Point out each Plasmodium parasite.
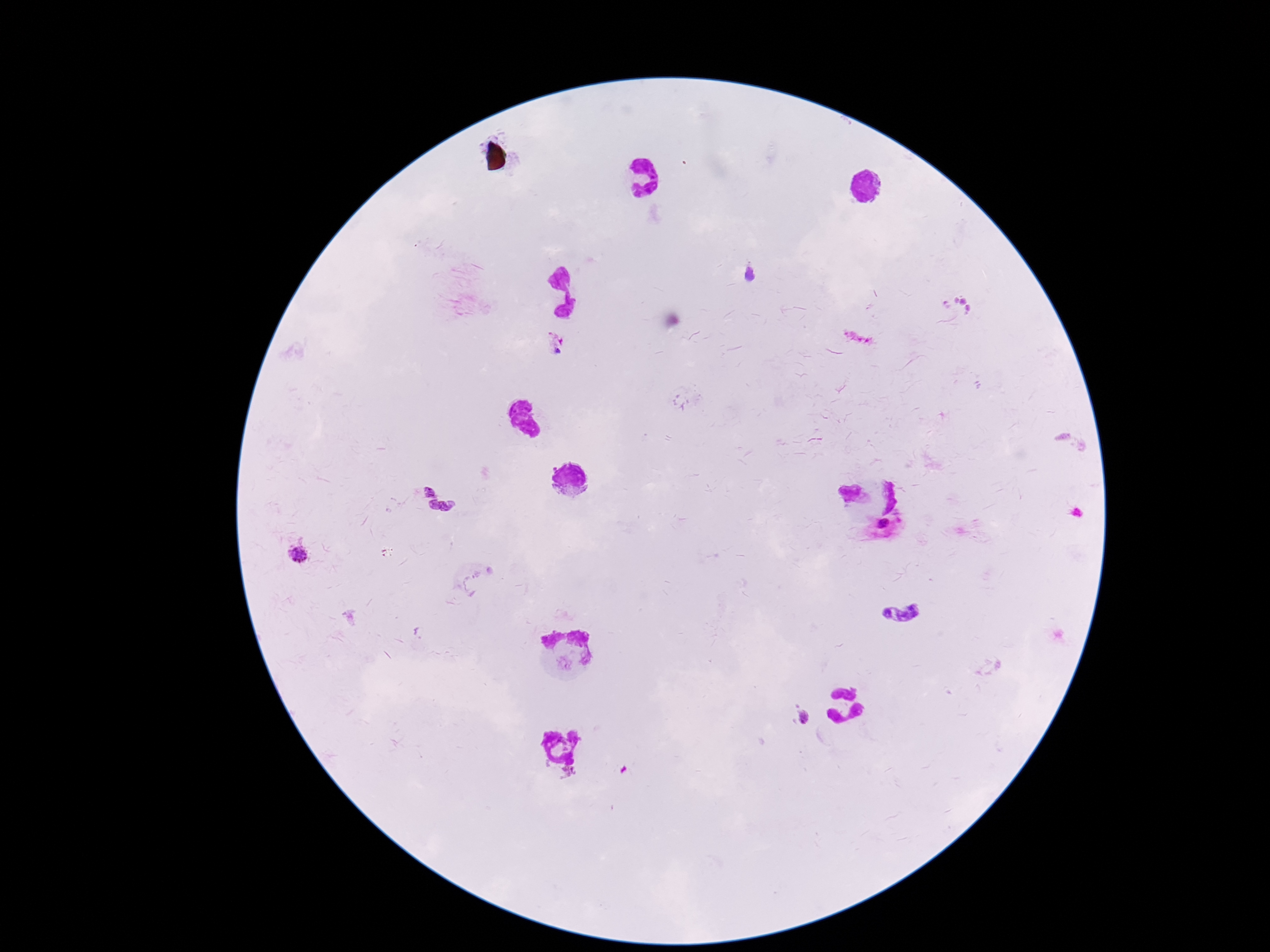

Approximate object centers, in pixels from the top-left corner.
Plasmodium parasites: (x=750, y=276), (x=958, y=303), (x=555, y=347), (x=430, y=488), (x=442, y=508), (x=297, y=556), (x=905, y=615), (x=805, y=714), (x=547, y=767), (x=570, y=775).

field_of_view: single
image_size: 1270×952 pixels
magnification: 100x
capture: smartphone camera through the microscope eyepiece
patient_malaria_status: infected
stain: Giemsa
preparation: thick blood film